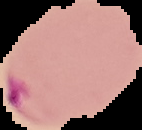
image size = 142×130 pixels
image type = cell region segmented out of the field of view; surrounding area masked to black
result = malaria parasites identified
preparation = thin blood smear